Look for parasitized red blood cells.
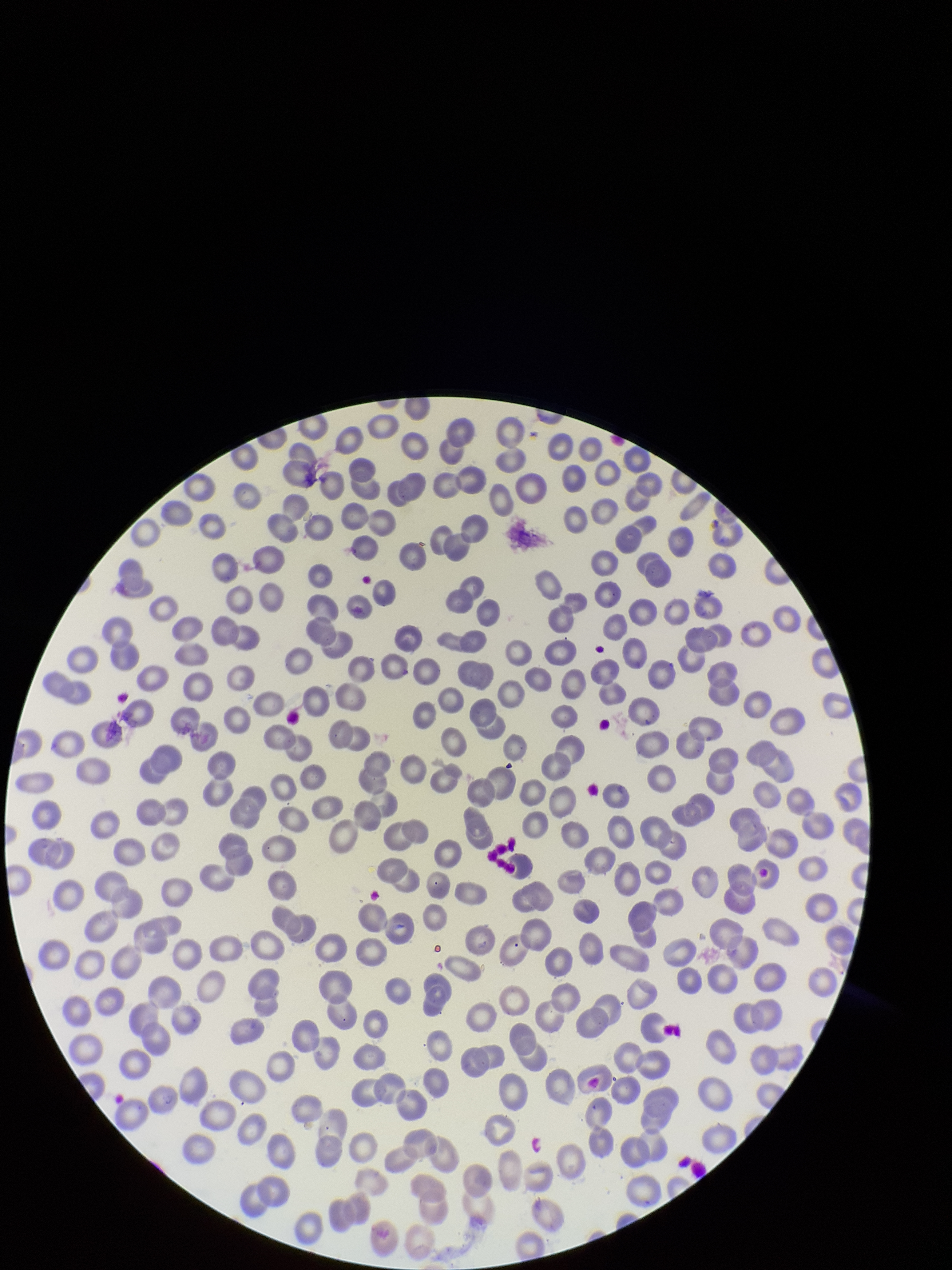

None seen.

Red blood cell count: 296. One field from this slide. Preparation: thin smear. Patient malaria status: negative. Parasitized red blood cell count: 0. Image is 952×1270 pixels. Stained with Giemsa. Smartphone photograph taken through the eyepiece of a microscope.